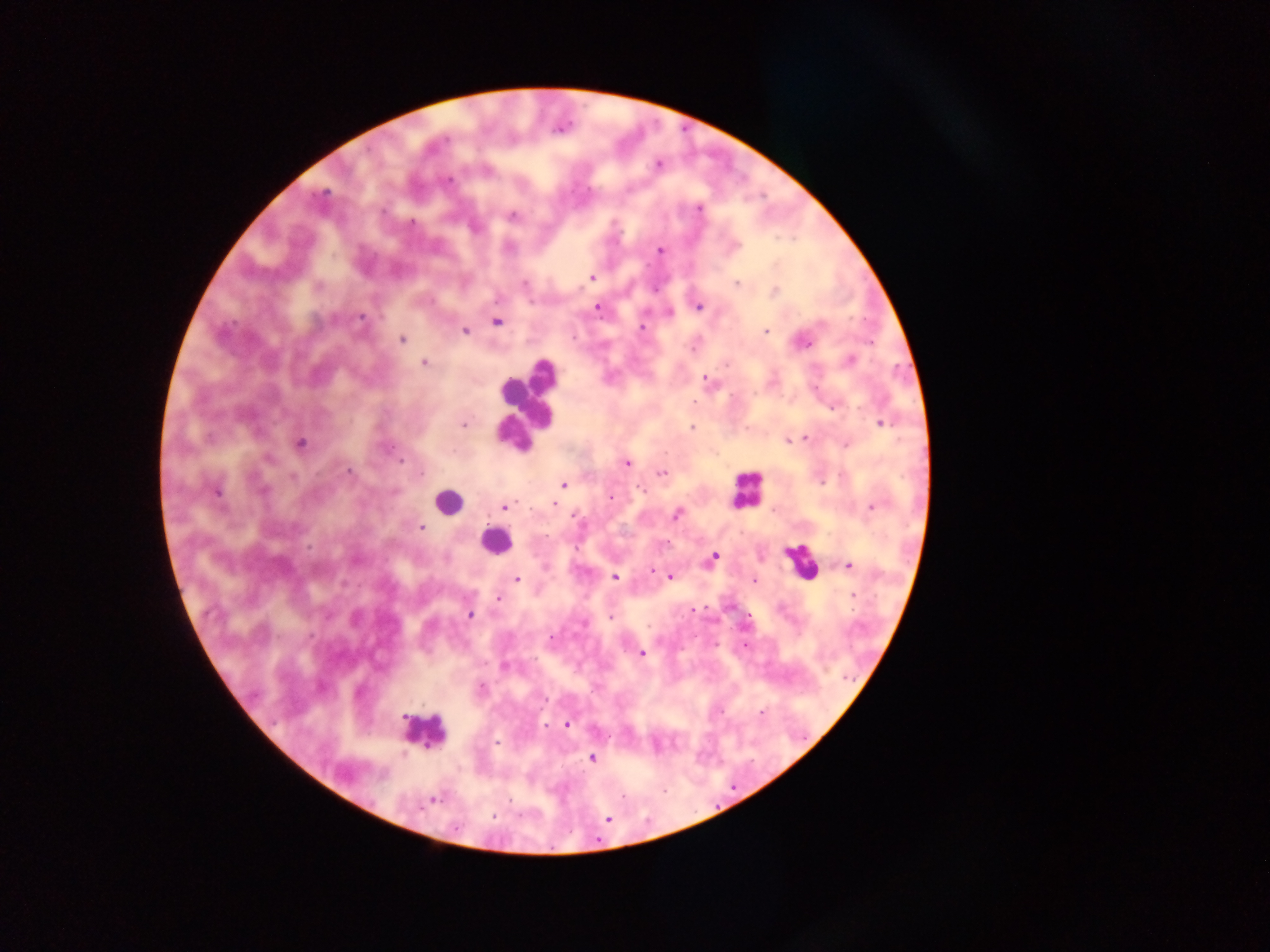
Approximate centers as [x, y] in pixels. Plasmodium parasite locations: [657, 165], [488, 171], [448, 181], [324, 192], [699, 208], [513, 215], [412, 222], [660, 251], [592, 278], [737, 283], [774, 291], [699, 307], [597, 308], [670, 312], [360, 317], [496, 322], [821, 325], [642, 327], [465, 331], [766, 332], [402, 339], [803, 342], [850, 360], [423, 363], [727, 365], [705, 379], [694, 402], [833, 408], [881, 424], [463, 425], [692, 428], [806, 437], [788, 440], [301, 443], [845, 445], [269, 459], [400, 461], [626, 463], [348, 471], [661, 473], [293, 477], [563, 484], [263, 491], [217, 492], [611, 498], [554, 504], [505, 507], [871, 507], [677, 514], [575, 516], [421, 527], [713, 558], [849, 565], [653, 572], [670, 576], [615, 577], [517, 579], [754, 580], [853, 595], [498, 600], [470, 615], [609, 617], [551, 638], [744, 645], [641, 653], [504, 667], [482, 687], [544, 699], [403, 717], [567, 725], [545, 727], [497, 743], [591, 759], [430, 801], [608, 818]. Leukocyte locations: [527, 403], [746, 487], [448, 501], [494, 540], [800, 561], [423, 731]. One field of view. Image is 1270×952 pixels. Mobile-phone photograph taken through the microscope. Thick blood smear. Collected in Ghana.